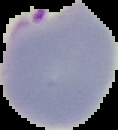
Summary:
  - Image size: 118×130 pixels
  - Malaria status: parasitized
  - Image type: segmented cell region with the area outside set to black
  - Preparation: thin blood smear